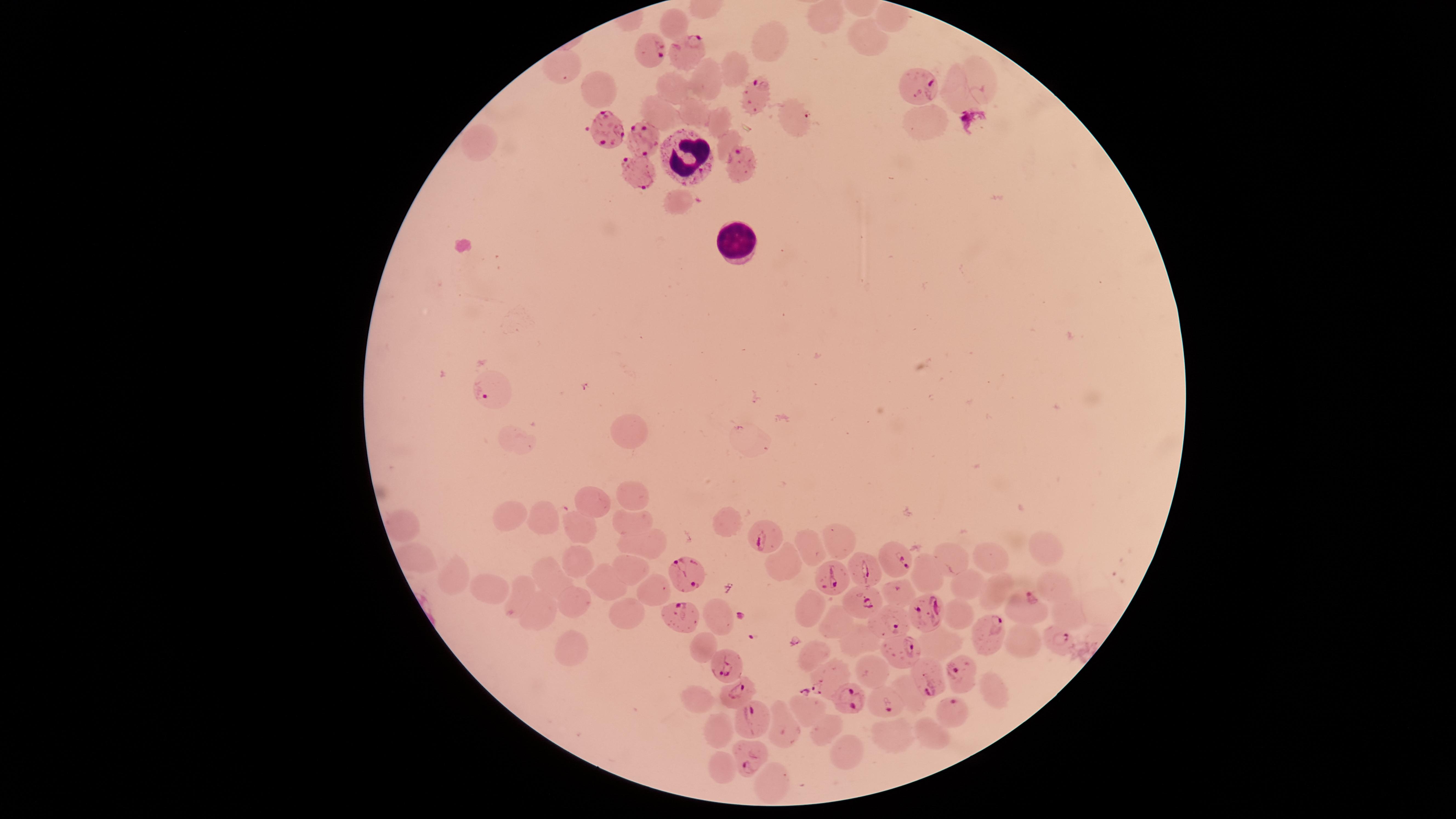

visible region = circular
capture = smartphone photograph through the microscope eyepiece
parasitized red blood cells = approximate marker points as [x, y] in pixels: [653, 48], [689, 52], [921, 86], [752, 93], [605, 129], [644, 136], [740, 167], [641, 176], [490, 392], [768, 539], [898, 559], [689, 570], [865, 571], [838, 581], [861, 600], [1031, 608], [925, 611], [674, 618], [890, 618], [989, 635], [1060, 638], [899, 653], [729, 667], [956, 674], [828, 677], [929, 680], [735, 691], [854, 702], [883, 703], [953, 711], [756, 719], [753, 760]
white blood cells = approximate marker points as [x, y] in pixels: [684, 152], [731, 239]
image size = 1456×819 pixels
presence = malaria parasites seen
stain = Giemsa
preparation = thin blood smear
species = Plasmodium falciparum
uninfected red blood cells = approximate marker points as [x, y] in pixels: [825, 17], [678, 21], [864, 38], [771, 42], [730, 65], [565, 66], [978, 79], [706, 81], [591, 87], [676, 88], [958, 94], [693, 107], [653, 108], [797, 115], [714, 120], [479, 140], [727, 140], [676, 201], [629, 435], [512, 441], [634, 493], [590, 502], [510, 518], [634, 519], [547, 521], [396, 523], [729, 524], [582, 528], [839, 540], [645, 544], [811, 552], [1047, 553], [951, 555], [578, 558], [990, 559], [416, 560], [781, 561], [632, 570], [456, 574], [551, 575], [931, 577], [605, 582], [1053, 583], [969, 588], [997, 588], [488, 590], [653, 590], [897, 594], [517, 596], [579, 601], [816, 607], [629, 611], [1067, 612], [542, 613], [958, 614], [716, 617], [836, 623], [857, 641], [1023, 642], [705, 645], [574, 647], [944, 649], [815, 651], [874, 668], [910, 690], [993, 690], [697, 700], [808, 709], [826, 729], [715, 730], [782, 730], [928, 732], [895, 737], [846, 753], [725, 766], [764, 787]
field of view = single